Report the malaria status of this cell.
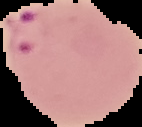
Parasitized.

From a thin blood smear. The area outside the segmented cell region is set to black. Image is 142×127 pixels.